Assess the morphology of the erythrocytes.
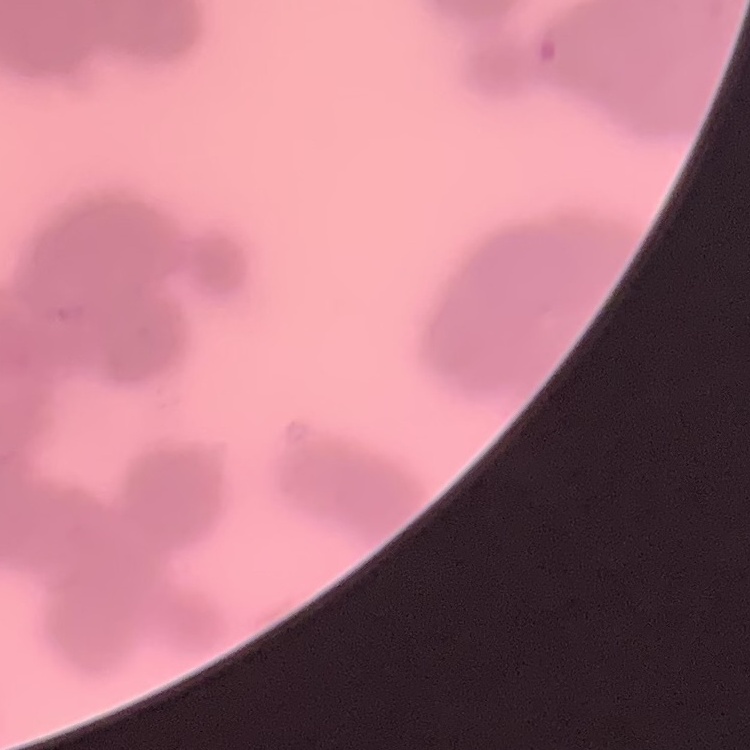
They show rouleaux formation.

Summary:
  - Image type: one tile cut from a larger photomicrograph
  - Stain: Field's or Giemsa
  - Preparation: thin blood smear